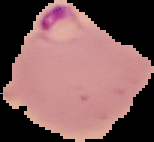
Summary:
  - Preparation: thin blood film
  - Result: Plasmodium parasites identified
  - Image size: 154×142 pixels
  - Image type: segmented cell region on a black background